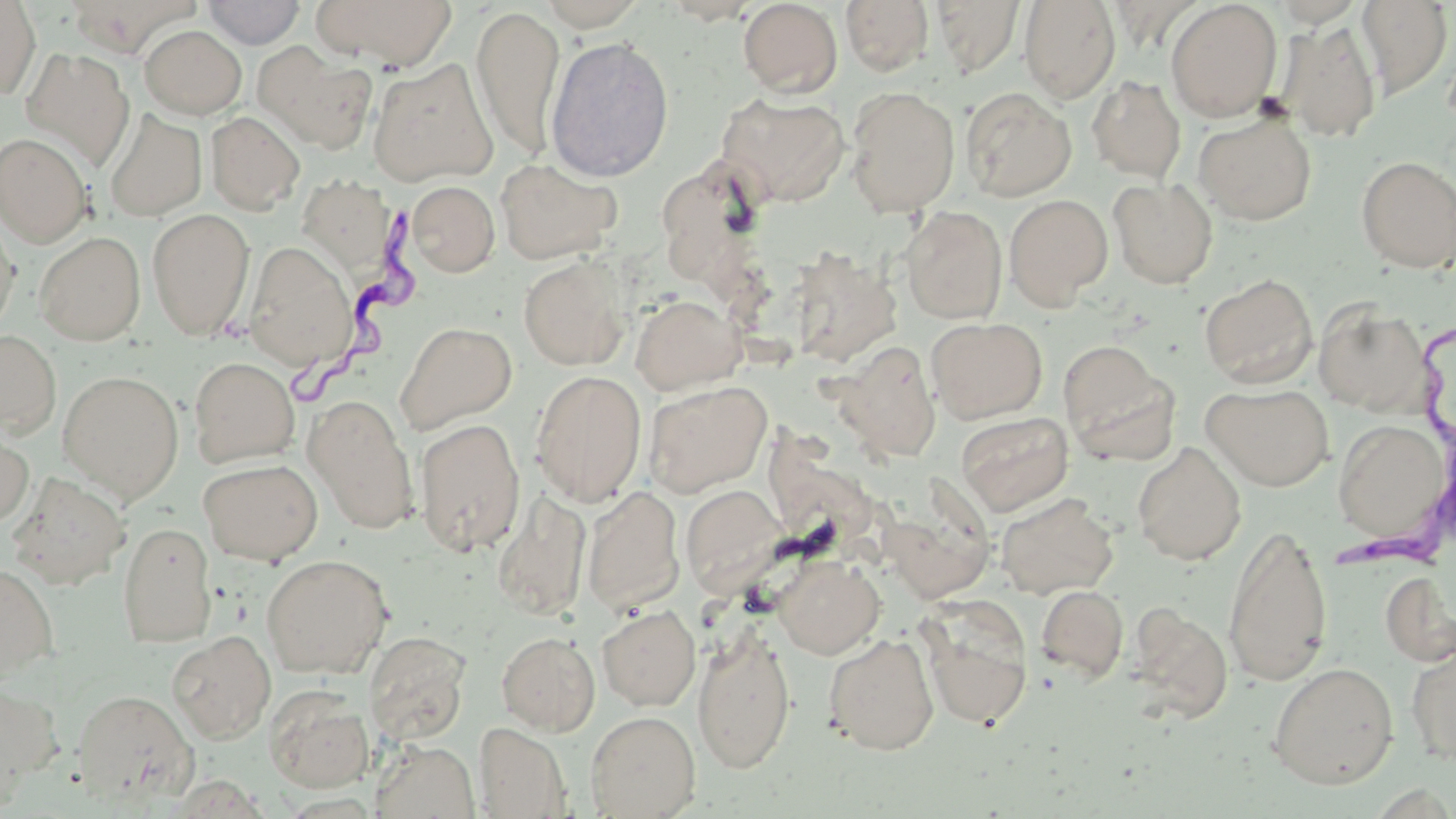
Approximate bounding boxes as (x1,y1)-(x2,y2) corner pairs in pixels. Uninfected red blood cell locations: (0,0)-(40,101), (202,0)-(306,48), (311,0)-(458,69), (539,0)-(649,30), (659,0)-(762,24), (840,0)-(934,76), (931,0)-(1025,77), (1019,0)-(1121,104), (1165,0)-(1283,121), (738,1)-(843,98), (1355,1)-(1453,99), (472,6)-(565,161), (1279,18)-(1382,142), (139,25)-(247,119), (545,35)-(675,182), (254,43)-(377,153), (21,47)-(134,170), (367,58)-(499,186), (1087,76)-(1186,183), (845,87)-(961,216), (960,87)-(1077,201), (716,92)-(850,207), (104,109)-(207,222), (206,111)-(305,214), (1193,113)-(1317,226), (0,133)-(92,248), (1356,155)-(1456,273), (495,156)-(623,264), (299,168)-(397,262), (1108,178)-(1218,289), (406,181)-(500,277), (1004,194)-(1113,308), (0,206)-(19,337), (900,206)-(1008,324), (147,208)-(255,341), (34,232)-(145,345), (245,239)-(358,371), (787,247)-(903,367), (519,257)-(631,370), (1199,273)-(1319,389), (630,294)-(747,395), (1313,301)-(1432,416), (926,317)-(1048,424), (395,321)-(517,434), (0,330)-(61,438), (834,340)-(941,463), (1058,341)-(1178,463), (189,356)-(299,468), (58,370)-(184,503), (530,370)-(647,507), (644,381)-(772,497), (1201,382)-(1335,491), (304,396)-(420,534), (956,411)-(1073,516), (415,418)-(526,557), (1333,418)-(1450,548), (0,425)-(34,531), (1132,442)-(1246,565), (198,458)-(323,565), (6,472)-(131,588), (681,484)-(786,593), (581,485)-(685,614), (492,491)-(592,622), (995,493)-(1118,599), (117,521)-(217,647), (1222,521)-(1333,689), (260,553)-(394,678), (773,556)-(884,659), (0,563)-(58,682), (1380,571)-(1456,668), (1035,584)-(1129,683), (916,597)-(1034,731), (597,604)-(701,710), (1128,604)-(1233,725), (692,628)-(796,775), (167,630)-(276,743), (496,631)-(600,735), (364,632)-(471,744), (823,632)-(939,755), (1404,641)-(1456,764), (1267,661)-(1399,789), (0,684)-(63,801), (264,685)-(375,793), (72,689)-(199,806), (586,710)-(700,818), (474,722)-(571,818), (371,740)-(480,819). Trypanosoma brucei locations: (294,190)-(433,401), (1339,330)-(1455,572). Slide-level diagnosis: Trypanosoma brucei. Thin blood film. Single field of view. Image is 1456×819 pixels. 1000x magnification. May-Grünwald-Giemsa stain. Optical microscopy.